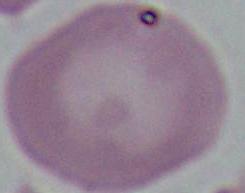
magnification = 1000x
modality = micrograph
identification = red blood cell